Describe the morphology of the red blood cells.
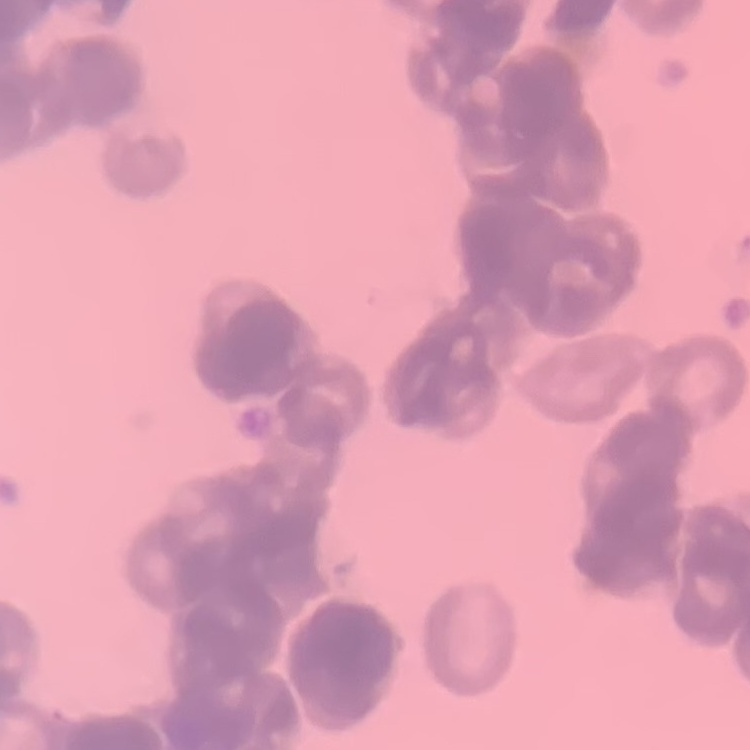

They show rouleaux formation.

Summary:
  - Preparation: thin blood film
  - Image type: one tile cut from a larger photomicrograph
  - Stain: Field's or Giemsa